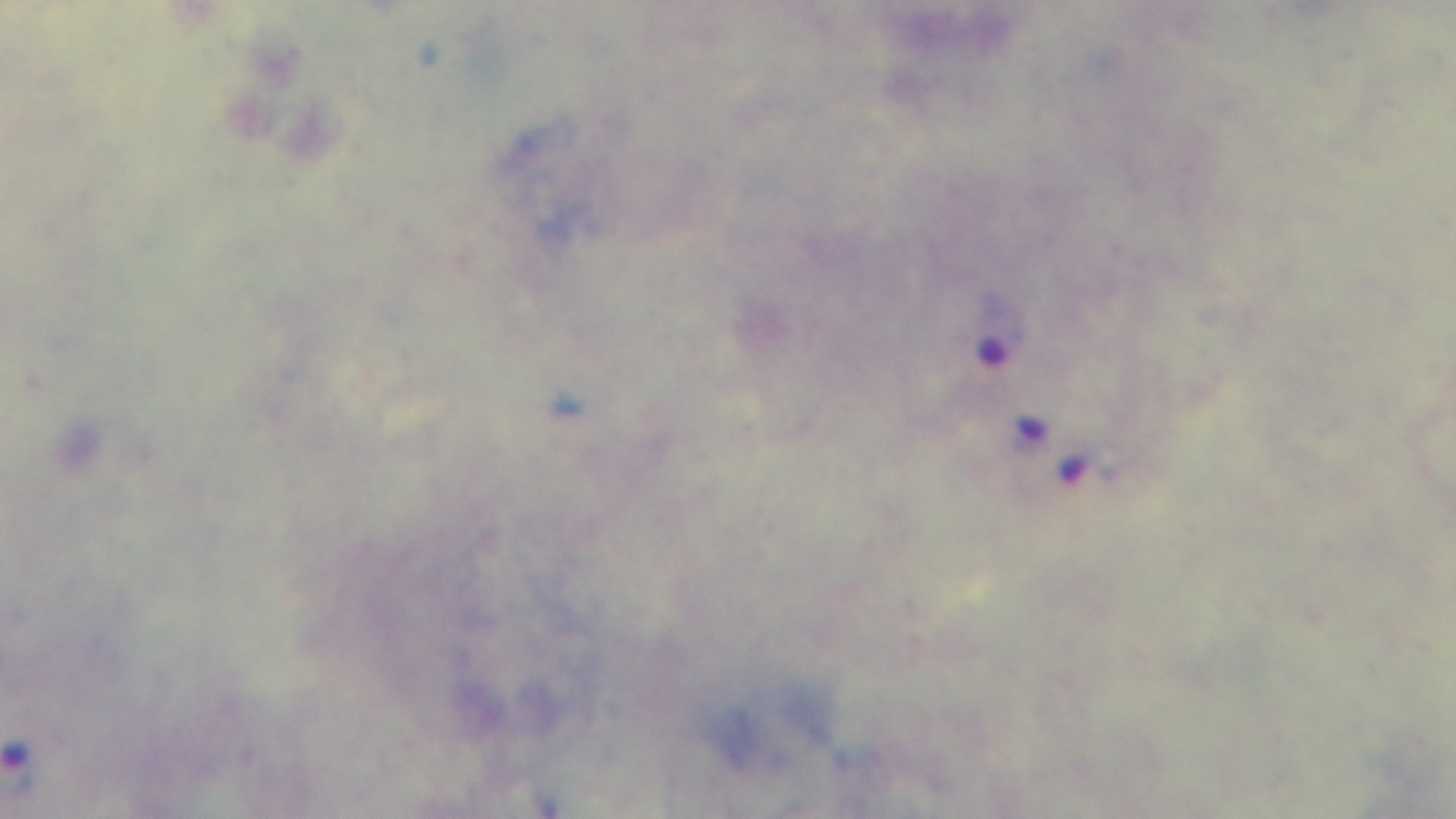
preparation = thick smear
objective = 100x oil immersion
capture = mounted 4K digital camera
modality = light microscopy
field of view = single
stain = Giemsa
malaria status = positive